Describe the morphology of the red blood cells.
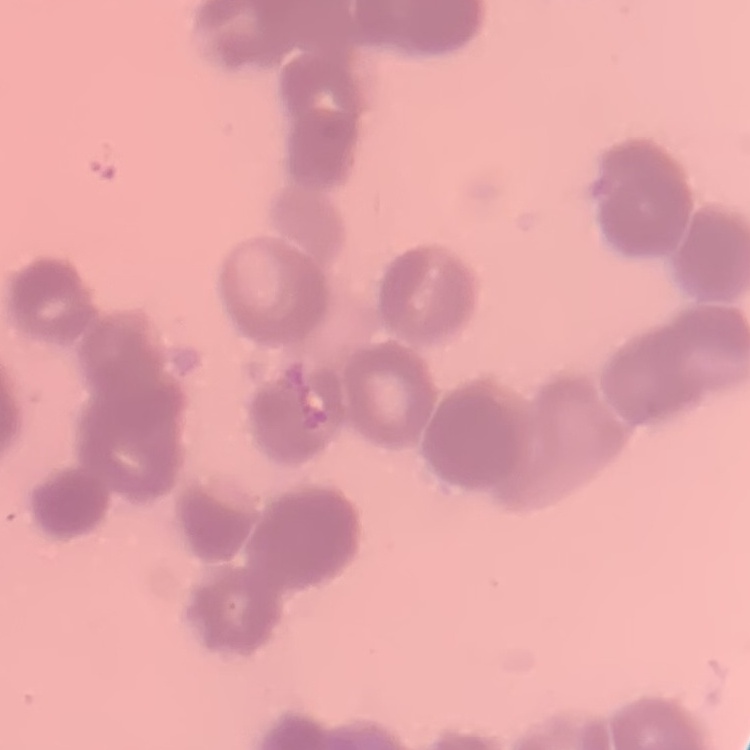
They show rouleaux formation.

Field's or Giemsa stain. Thin blood film. One tile cut from a larger photomicrograph.